State which cell type is depicted.
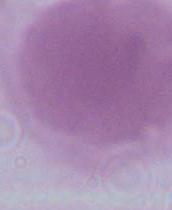
This is an erythrocyte.

Summary:
  - Magnification: 1000x
  - Modality: micrograph